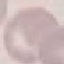

Result: no malaria parasites seen. Photographed with a smartphone camera at the microscope eyepiece. Giemsa stain. Thin blood smear. Automatically extracted cell patch, resized to 64 × 64 pixels.